Identify the parasite.
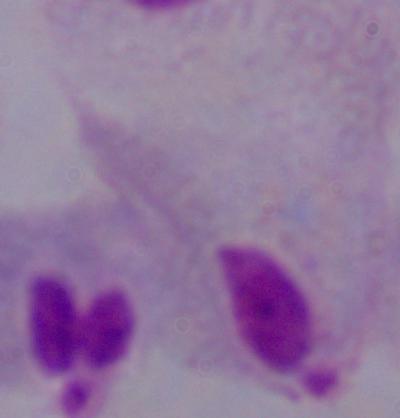
A trichomonad.

Summary:
  - Magnification: 1000x
  - Modality: micrograph